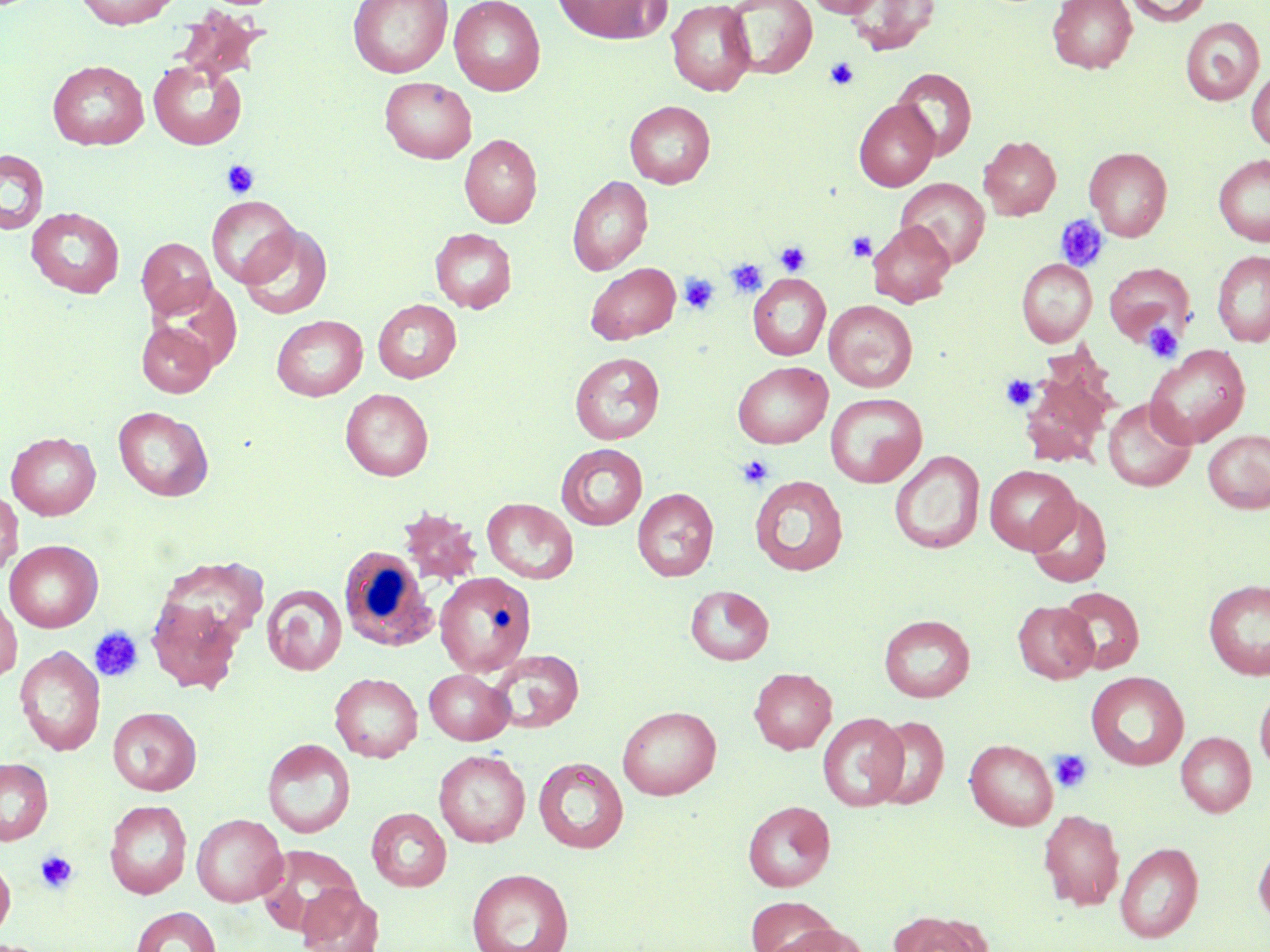

slide-level diagnosis = negative for blood parasites
white blood cell locations = approximate bounding boxes as (x1, y1, x2, y2) in pixels: (338, 546, 438, 653)
platelet locations = approximate bounding boxes as (x1, y1, x2, y2) in pixels: (824, 58, 860, 91), (220, 160, 259, 198), (1054, 214, 1109, 273), (847, 232, 877, 262), (775, 240, 811, 277), (727, 259, 767, 297), (678, 273, 719, 314), (1142, 322, 1182, 361), (1001, 374, 1038, 410), (737, 454, 774, 488), (89, 627, 143, 682), (1050, 749, 1093, 793), (35, 850, 79, 893)
preparation = thin blood smear
magnification = 1000x
modality = light microscopy
stain = May-Grünwald-Giemsa
uninfected red blood cell locations = approximate bounding boxes as (x1, y1, x2, y2) in pixels: (74, 0, 180, 29), (348, 0, 453, 78), (449, 0, 546, 95), (551, 0, 671, 44), (805, 0, 887, 17), (845, 0, 940, 55), (1048, 0, 1137, 73), (1125, 0, 1212, 26), (666, 1, 756, 96), (725, 1, 817, 79), (174, 7, 272, 85), (1181, 18, 1265, 105), (47, 60, 149, 150), (149, 60, 247, 150), (1247, 66, 1270, 150), (892, 68, 977, 160), (379, 77, 477, 163), (853, 99, 939, 191), (624, 100, 715, 188), (459, 134, 542, 227), (979, 135, 1061, 220), (1084, 147, 1172, 241), (0, 149, 49, 235), (1214, 153, 1270, 246), (567, 175, 653, 275), (896, 178, 989, 268), (206, 196, 300, 288), (26, 207, 125, 298), (867, 220, 955, 308), (238, 225, 332, 319), (430, 228, 517, 313), (137, 237, 217, 319), (1212, 250, 1270, 347), (1017, 258, 1097, 347), (585, 262, 680, 344), (1103, 262, 1196, 346), (748, 273, 830, 360), (373, 299, 462, 383), (824, 300, 918, 392), (272, 315, 368, 401), (137, 321, 216, 397), (1146, 344, 1250, 448), (570, 352, 664, 444), (733, 361, 833, 449), (1019, 367, 1113, 468), (340, 388, 433, 481), (825, 392, 927, 487), (1102, 398, 1196, 492), (113, 406, 213, 501), (1203, 430, 1270, 513), (6, 432, 101, 520), (556, 444, 648, 530), (889, 450, 985, 555), (984, 465, 1080, 554), (750, 475, 848, 576), (632, 488, 719, 581), (0, 490, 22, 577), (1026, 494, 1112, 588), (482, 498, 578, 584), (396, 506, 482, 587), (5, 540, 102, 632), (151, 554, 264, 664), (434, 572, 536, 678), (1203, 579, 1270, 681), (262, 585, 347, 676), (685, 585, 774, 665), (1057, 586, 1145, 674), (0, 592, 21, 683), (145, 592, 246, 696), (1012, 601, 1098, 683), (879, 614, 975, 702), (15, 646, 105, 756), (486, 648, 585, 733), (749, 667, 837, 754), (424, 669, 514, 745), (1086, 671, 1189, 770), (330, 672, 423, 762), (1255, 685, 1270, 774), (617, 705, 722, 800), (108, 706, 202, 795), (818, 712, 908, 810), (870, 715, 949, 809), (1176, 731, 1257, 817), (965, 738, 1058, 830), (263, 739, 355, 838), (434, 749, 529, 847), (0, 757, 53, 845), (533, 757, 629, 854), (104, 799, 192, 899), (742, 800, 836, 892), (366, 807, 452, 891), (1039, 808, 1125, 910), (192, 814, 287, 906), (1253, 840, 1270, 926), (1115, 842, 1203, 943), (259, 845, 361, 937), (0, 853, 15, 943), (466, 867, 574, 952), (296, 884, 384, 952), (745, 896, 842, 951), (130, 906, 221, 952), (890, 910, 992, 952), (768, 923, 872, 952)
image size = 1270×952 pixels
field of view = single